Classify this cell by malaria status.
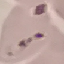
It is uninfected.

Summary:
  - Capture: smartphone through the microscope eyepiece
  - Preparation: thin blood smear
  - Image type: automatically extracted cell patch, resized to 64 × 64 pixels
  - Stain: Giemsa